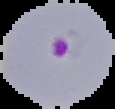
Summary:
  - Image type: segmented cell region with the area outside set to black
  - Image size: 115×109 pixels
  - Malaria status: parasitized
  - Preparation: thin blood film